Point out each malaria parasite and each leukocyte.
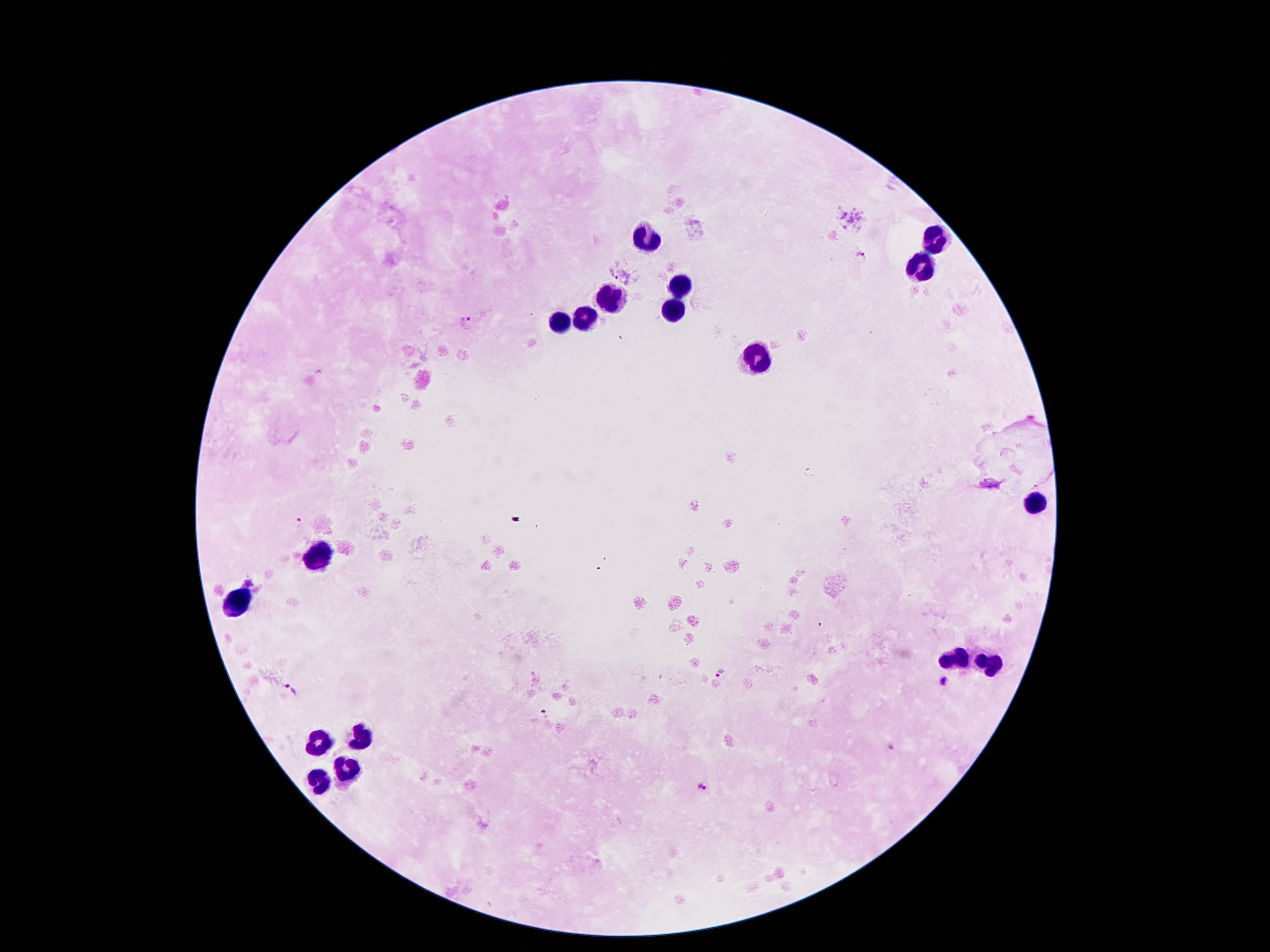
Approximate centers as (x, y) in pixels.
Malaria parasites: (860, 255), (612, 272), (469, 321), (301, 523), (722, 675), (944, 683), (288, 689), (544, 713), (892, 749), (703, 785).
Leukocytes: (646, 238), (930, 238), (925, 269), (681, 286), (615, 299), (670, 308), (584, 319), (561, 322), (757, 354), (1033, 502), (318, 555), (241, 600), (956, 658), (988, 662), (363, 738), (321, 742), (345, 772), (318, 781).

patient malaria status = positive for Plasmodium falciparum
field of view = one from this slide
preparation = thick peripheral-blood smear
capture = smartphone camera through the microscope eyepiece
image size = 1270×952 pixels
magnification = 100x
stain = Giemsa